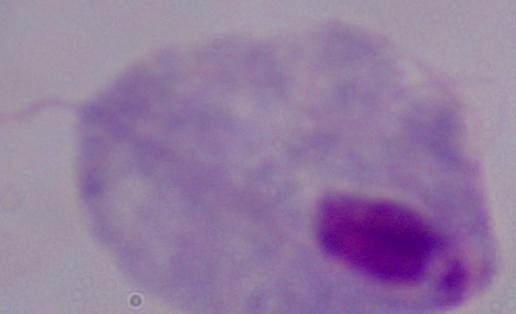

magnification: 1000x
modality: micrograph
identification: trichomonad